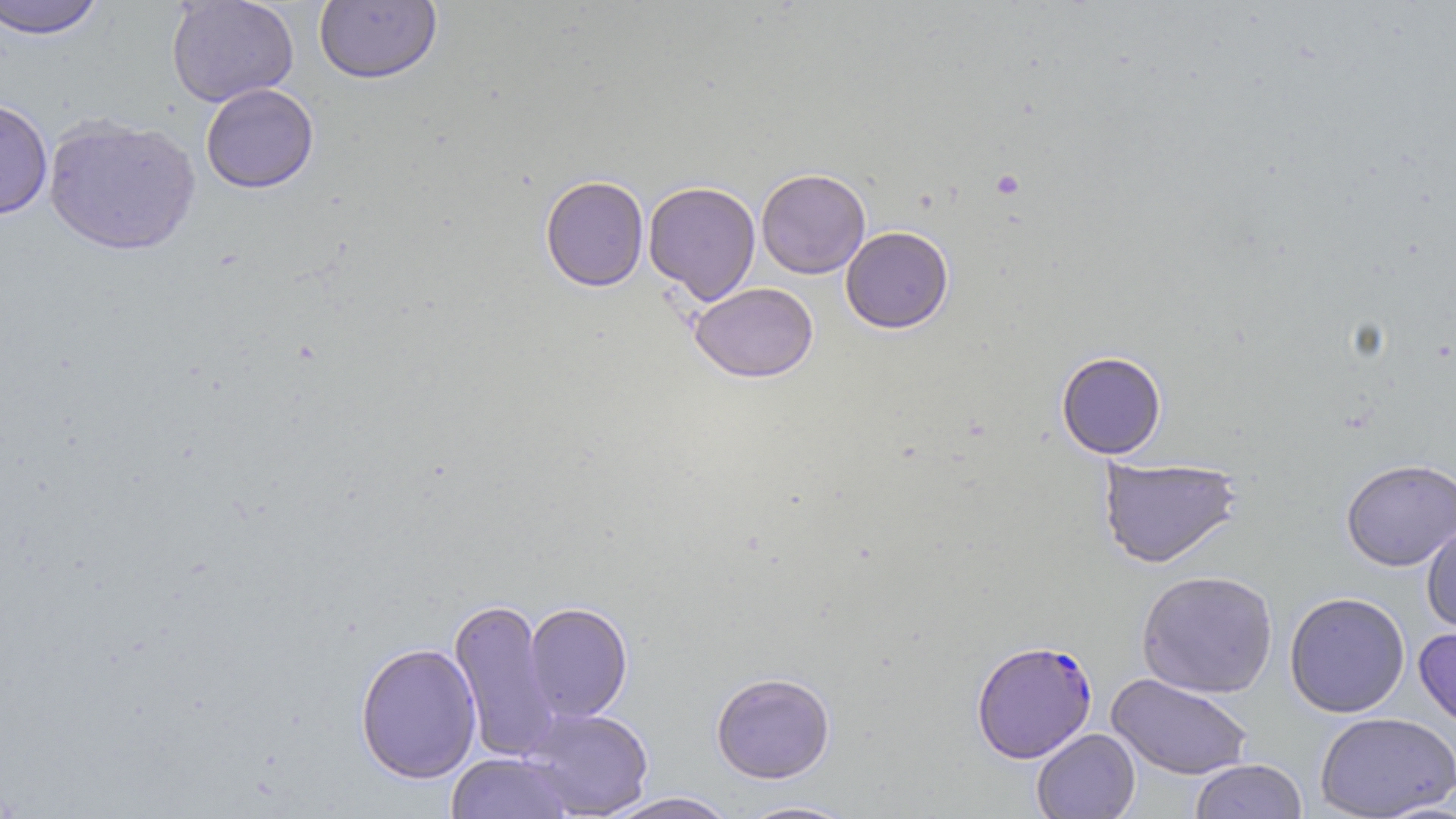 Approximate bounding boxes as (x1, y1, x2, y2) in pixels. Uninfected red blood cell locations: (0, 0, 106, 40), (166, 0, 299, 107), (314, 1, 442, 85), (200, 83, 319, 194), (0, 97, 52, 221), (43, 116, 200, 256), (756, 168, 870, 278), (540, 175, 649, 291), (643, 180, 761, 304), (840, 226, 953, 333), (689, 282, 819, 382), (1056, 351, 1167, 459), (1098, 456, 1243, 569), (1340, 457, 1456, 571), (1421, 524, 1456, 635), (1136, 570, 1278, 699), (1284, 591, 1411, 718), (448, 597, 561, 763), (524, 602, 633, 722), (1414, 625, 1456, 732), (354, 642, 482, 784), (711, 672, 836, 784), (1107, 673, 1254, 780), (520, 706, 654, 818), (1315, 711, 1455, 818), (1031, 728, 1140, 818), (446, 752, 575, 819), (1189, 759, 1307, 818), (604, 792, 740, 819), (734, 799, 862, 818). Plasmodium falciparum-infected red blood cell locations: (971, 639, 1097, 763). Slide-level diagnosis: Plasmodium falciparum. Image is 1456×819 pixels. One field of a larger specimen. Light microscopy. Thin blood smear. Captured at 1000x magnification. May-Grünwald-Giemsa-stained preparation.